Give the extent of all Plasmodium falciparum-infected red blood cells.
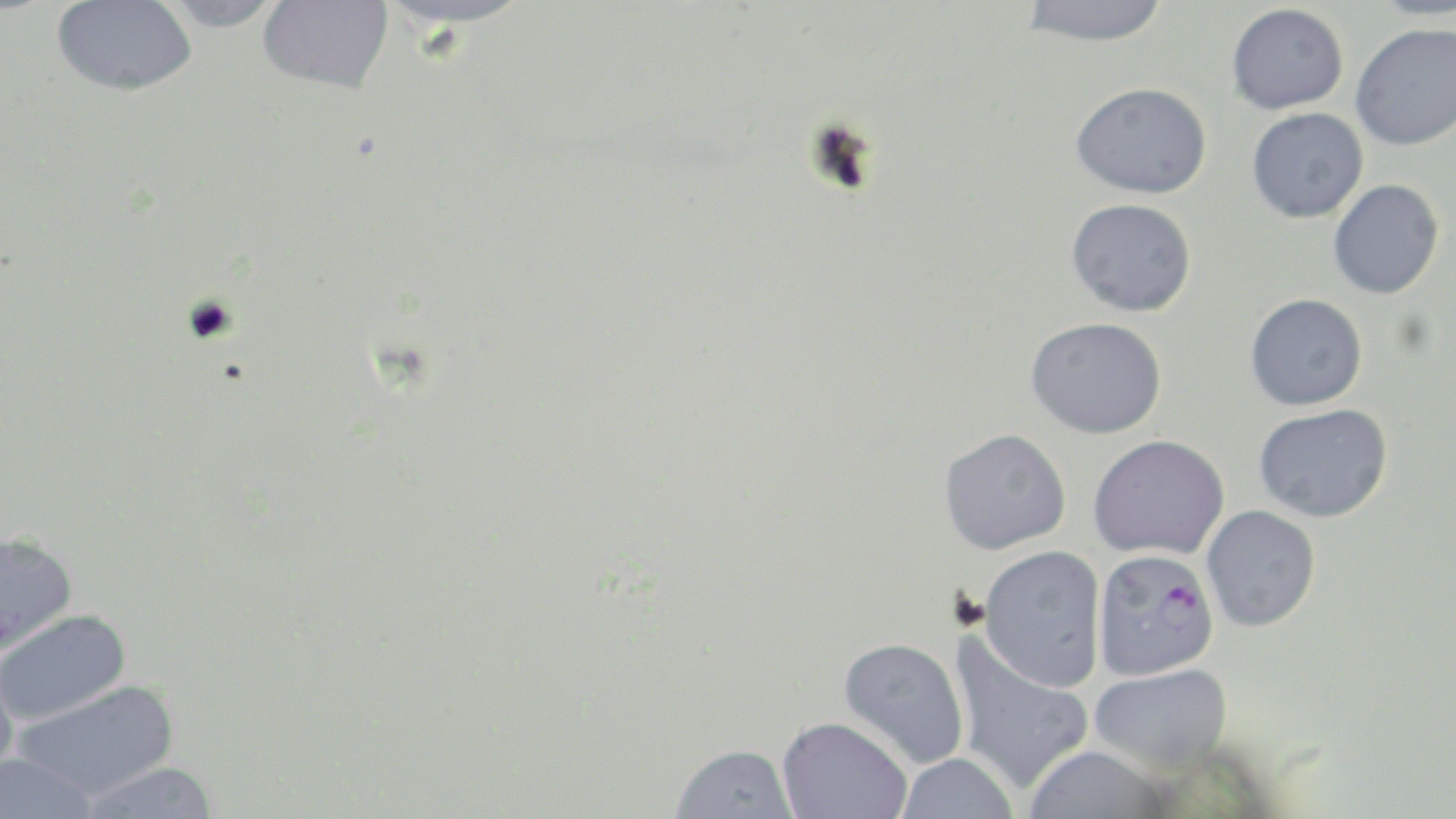

Approximate bounding boxes as (x1,y1)-(x2,y2) corner pairs in pixels.
Plasmodium falciparum-infected red blood cells: (1092,548)-(1219,681).

Summary:
  - Uninfected red blood cell locations: (51,0)-(198,98), (153,0)-(288,32), (256,0)-(394,95), (376,0)-(541,28), (1019,0)-(1170,47), (1367,0)-(1455,20), (1226,3)-(1349,115), (1350,22)-(1456,151), (1070,82)-(1212,200), (1246,107)-(1368,223), (1328,179)-(1444,299), (1066,198)-(1197,317), (1244,293)-(1368,411), (1025,317)-(1168,439), (1253,403)-(1393,523), (938,428)-(1072,554), (1088,434)-(1230,560), (1201,504)-(1321,632), (0,530)-(78,657), (978,545)-(1107,692), (1,609)-(133,727), (947,634)-(1094,795), (838,637)-(970,770), (0,655)-(21,792), (1088,664)-(1233,775), (12,679)-(179,802), (776,716)-(912,818), (670,743)-(799,819), (1022,746)-(1176,819), (0,752)-(101,819), (894,752)-(1019,819), (76,761)-(221,818)
  - Slide-level diagnosis: Plasmodium falciparum
  - Preparation: thin blood film
  - Modality: optical microscopy
  - Magnification: 1000x
  - Stain: May-Grünwald-Giemsa
  - Image size: 1456×819 pixels
  - Field of view: single